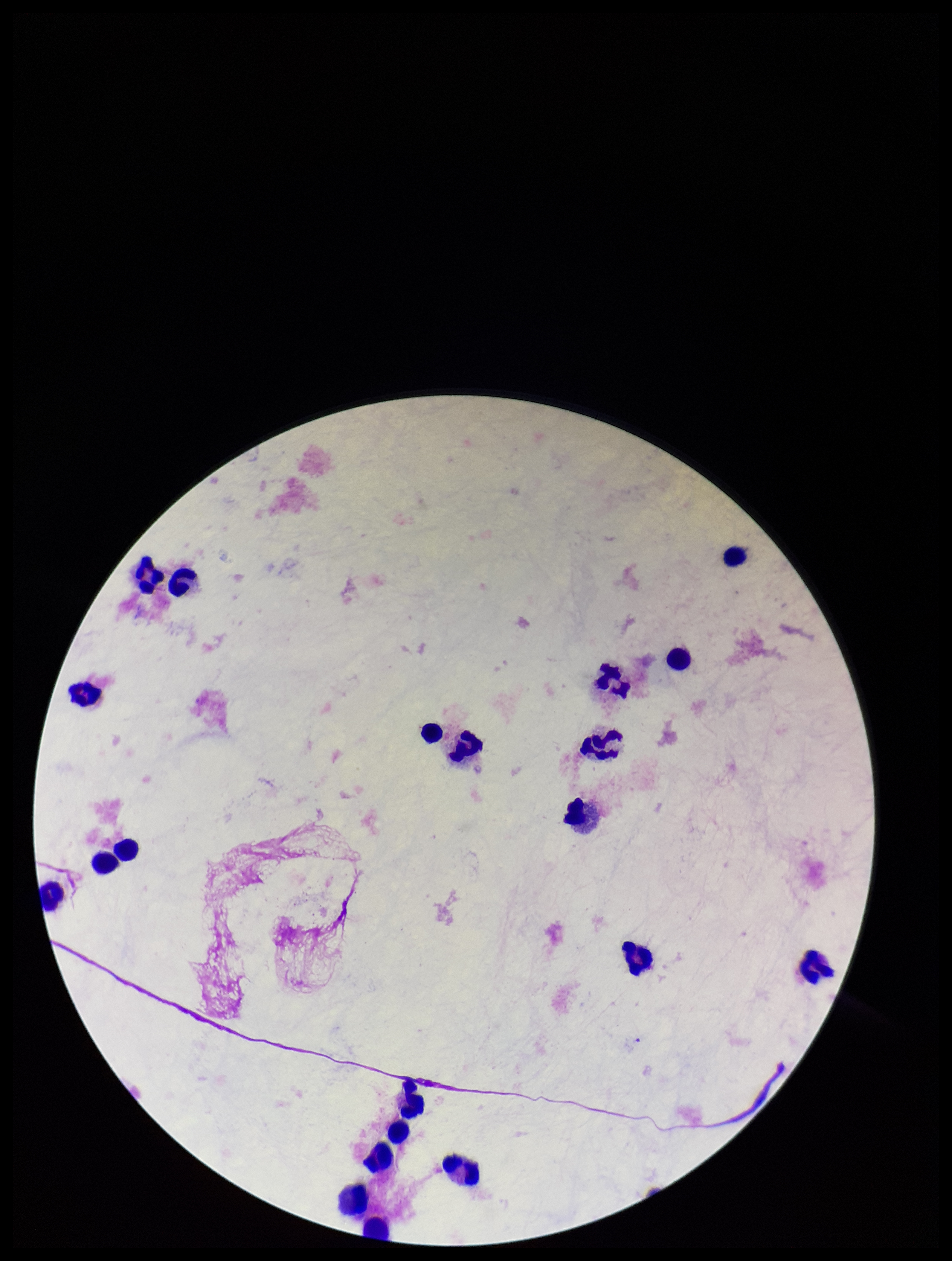

Summary:
  - Capture: smartphone photograph through the microscope eyepiece
  - Plasmodium parasites: none identified
  - Image size: 952×1261 pixels
  - Stain: Giemsa
  - Leukocyte count: 21
  - Parasite count: 0
  - Patient malaria status: negative
  - Field of view: single
  - Preparation: thick smear